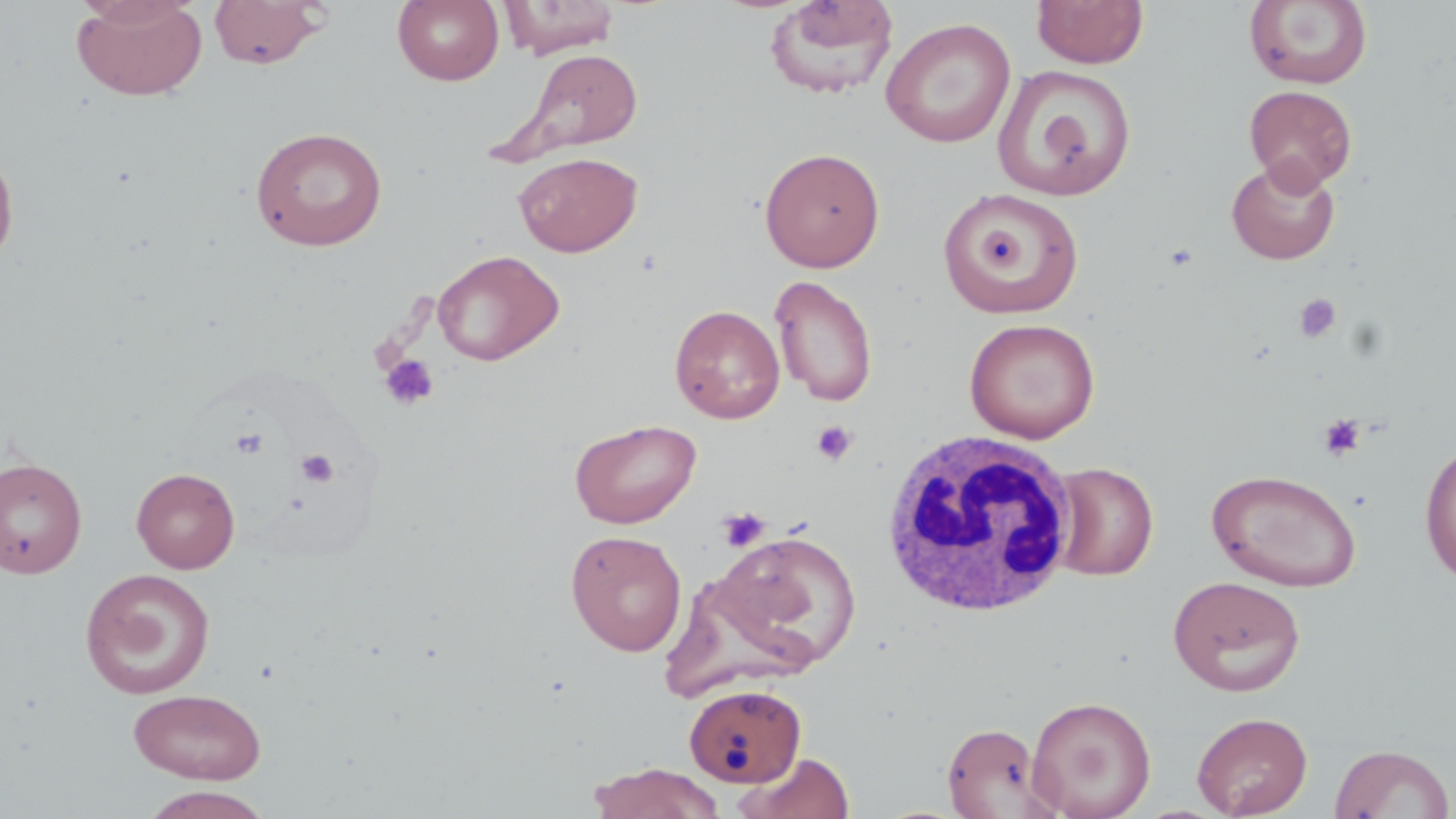
Summary:
  - Coordinate format: approximate bounding boxes as [x1, y1, x2, y2] in pixels
  - Platelet locations: [1294, 293, 1342, 344], [379, 353, 439, 411], [1319, 413, 1365, 461], [812, 420, 858, 466], [230, 427, 269, 459], [296, 449, 339, 488], [717, 507, 771, 552]
  - Uninfected red blood cell locations: [71, 0, 208, 102], [208, 0, 327, 69], [393, 0, 504, 86], [499, 0, 620, 59], [763, 0, 899, 99], [1032, 0, 1148, 68], [1244, 0, 1373, 89], [881, 17, 1016, 148], [515, 47, 644, 157], [993, 64, 1136, 201], [1243, 85, 1358, 192], [250, 126, 387, 251], [0, 139, 19, 273], [759, 146, 885, 272], [514, 151, 642, 257], [1226, 158, 1340, 265], [938, 186, 1084, 319], [432, 249, 565, 366], [769, 274, 879, 407], [669, 304, 785, 424], [964, 317, 1100, 444], [570, 418, 701, 529], [1419, 439, 1456, 588], [0, 457, 87, 579], [1047, 462, 1159, 581], [131, 467, 240, 573], [1206, 468, 1363, 593], [565, 530, 687, 656], [709, 530, 862, 670], [79, 567, 217, 700], [1168, 575, 1306, 697], [683, 683, 806, 788], [128, 688, 267, 784], [1026, 695, 1157, 818], [1191, 711, 1313, 818], [941, 722, 1059, 819], [1329, 743, 1454, 819], [733, 751, 855, 819], [588, 763, 725, 819], [137, 786, 274, 819]
  - White blood cell locations: [880, 427, 1080, 617]
  - Slide-level diagnosis: no evidence of blood parasites
  - Field of view: single
  - Modality: light microscopy
  - Magnification: 1000x
  - Preparation: thin blood smear
  - Stain: May-Grünwald-Giemsa
  - Image size: 1456×819 pixels